Locate every blood parasite and identify its species.
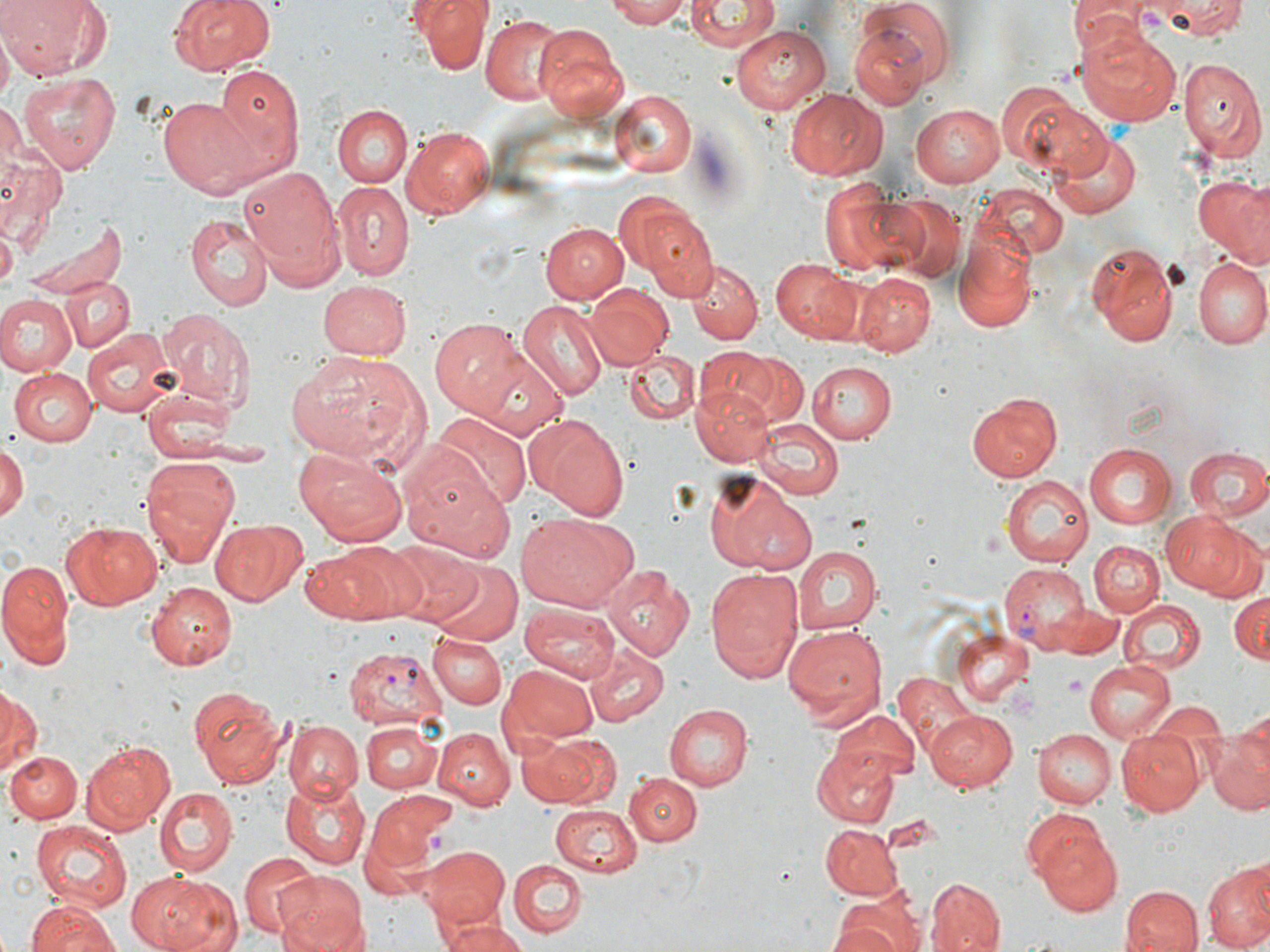

Approximate bounding boxes as named x1/y1/x2/y2 corners in pixels.
Plasmodium vivax-infected red blood cells: (x1=850, y1=26, x2=933, y2=109), (x1=999, y1=562, x2=1089, y2=648), (x1=343, y1=645, x2=447, y2=726).
No Plasmodium falciparum, Plasmodium ovale, Plasmodium malariae, Babesia divergens, or Trypanosoma brucei observed.

Summary:
  - Uninfected red blood cell locations: (x1=0, y1=0, x2=104, y2=79), (x1=169, y1=0, x2=277, y2=76), (x1=415, y1=0, x2=488, y2=74), (x1=604, y1=0, x2=691, y2=27), (x1=685, y1=0, x2=778, y2=50), (x1=1068, y1=0, x2=1147, y2=54), (x1=1145, y1=0, x2=1247, y2=39), (x1=860, y1=2, x2=959, y2=90), (x1=483, y1=16, x2=563, y2=104), (x1=536, y1=22, x2=628, y2=120), (x1=1077, y1=26, x2=1181, y2=128), (x1=732, y1=27, x2=829, y2=113), (x1=1178, y1=54, x2=1268, y2=164), (x1=213, y1=63, x2=305, y2=177), (x1=19, y1=72, x2=121, y2=174), (x1=994, y1=81, x2=1102, y2=176), (x1=786, y1=87, x2=890, y2=182), (x1=613, y1=89, x2=694, y2=174), (x1=158, y1=97, x2=262, y2=197), (x1=0, y1=101, x2=30, y2=184), (x1=910, y1=104, x2=1005, y2=186), (x1=333, y1=105, x2=412, y2=187), (x1=334, y1=112, x2=487, y2=198), (x1=401, y1=125, x2=496, y2=218), (x1=1048, y1=130, x2=1140, y2=221), (x1=0, y1=149, x2=67, y2=243), (x1=236, y1=165, x2=344, y2=285), (x1=1191, y1=173, x2=1268, y2=266), (x1=331, y1=183, x2=414, y2=282), (x1=820, y1=183, x2=918, y2=276), (x1=975, y1=184, x2=1068, y2=263), (x1=613, y1=189, x2=697, y2=275), (x1=882, y1=195, x2=966, y2=280), (x1=186, y1=212, x2=273, y2=311), (x1=22, y1=215, x2=132, y2=304), (x1=647, y1=216, x2=719, y2=296), (x1=541, y1=221, x2=629, y2=304), (x1=1, y1=226, x2=17, y2=285), (x1=953, y1=236, x2=1038, y2=334), (x1=1088, y1=241, x2=1179, y2=349), (x1=770, y1=258, x2=864, y2=345), (x1=685, y1=259, x2=762, y2=345), (x1=1192, y1=259, x2=1268, y2=350), (x1=853, y1=272, x2=936, y2=355), (x1=62, y1=277, x2=133, y2=350), (x1=317, y1=281, x2=411, y2=361), (x1=584, y1=284, x2=672, y2=370), (x1=0, y1=296, x2=76, y2=376), (x1=516, y1=301, x2=607, y2=401), (x1=156, y1=305, x2=254, y2=409), (x1=429, y1=317, x2=525, y2=416), (x1=83, y1=326, x2=177, y2=417), (x1=466, y1=345, x2=569, y2=440), (x1=625, y1=348, x2=700, y2=424), (x1=692, y1=348, x2=783, y2=424), (x1=285, y1=350, x2=425, y2=467), (x1=728, y1=351, x2=808, y2=427), (x1=806, y1=360, x2=897, y2=444), (x1=9, y1=369, x2=97, y2=445), (x1=694, y1=383, x2=774, y2=466), (x1=140, y1=389, x2=239, y2=462), (x1=963, y1=392, x2=1062, y2=483), (x1=429, y1=412, x2=530, y2=514), (x1=758, y1=420, x2=842, y2=498), (x1=534, y1=421, x2=628, y2=521), (x1=1086, y1=442, x2=1175, y2=529), (x1=0, y1=443, x2=26, y2=524), (x1=1185, y1=447, x2=1270, y2=521), (x1=295, y1=449, x2=407, y2=549), (x1=140, y1=460, x2=238, y2=566), (x1=401, y1=462, x2=519, y2=563), (x1=704, y1=473, x2=816, y2=575), (x1=1003, y1=474, x2=1096, y2=565), (x1=1163, y1=510, x2=1259, y2=596), (x1=516, y1=514, x2=629, y2=612), (x1=211, y1=518, x2=307, y2=608), (x1=61, y1=521, x2=162, y2=609), (x1=1089, y1=539, x2=1164, y2=617), (x1=335, y1=542, x2=433, y2=620), (x1=386, y1=542, x2=480, y2=623), (x1=298, y1=544, x2=400, y2=625), (x1=791, y1=547, x2=878, y2=634), (x1=0, y1=559, x2=72, y2=664), (x1=428, y1=561, x2=521, y2=645), (x1=602, y1=565, x2=695, y2=660), (x1=704, y1=566, x2=803, y2=682), (x1=147, y1=581, x2=242, y2=671), (x1=1229, y1=591, x2=1269, y2=665), (x1=1121, y1=597, x2=1204, y2=673), (x1=521, y1=604, x2=620, y2=682), (x1=1056, y1=607, x2=1123, y2=656), (x1=783, y1=622, x2=888, y2=730), (x1=952, y1=627, x2=1034, y2=707), (x1=429, y1=633, x2=506, y2=709), (x1=584, y1=646, x2=669, y2=725), (x1=1085, y1=658, x2=1176, y2=739), (x1=501, y1=666, x2=598, y2=743), (x1=891, y1=672, x2=977, y2=768), (x1=186, y1=683, x2=288, y2=786), (x1=0, y1=688, x2=40, y2=775), (x1=1145, y1=702, x2=1231, y2=737), (x1=663, y1=704, x2=752, y2=790), (x1=828, y1=709, x2=923, y2=784), (x1=928, y1=709, x2=1018, y2=792), (x1=283, y1=722, x2=364, y2=803), (x1=361, y1=722, x2=443, y2=794), (x1=1031, y1=728, x2=1115, y2=808), (x1=432, y1=729, x2=513, y2=809), (x1=1118, y1=731, x2=1204, y2=814), (x1=526, y1=734, x2=621, y2=808), (x1=1208, y1=736, x2=1270, y2=815), (x1=82, y1=740, x2=175, y2=831), (x1=813, y1=743, x2=904, y2=827), (x1=4, y1=751, x2=80, y2=823), (x1=626, y1=772, x2=702, y2=848), (x1=279, y1=779, x2=372, y2=868), (x1=154, y1=788, x2=237, y2=874), (x1=368, y1=792, x2=458, y2=872), (x1=551, y1=804, x2=644, y2=877), (x1=32, y1=820, x2=133, y2=911), (x1=821, y1=825, x2=904, y2=899), (x1=1032, y1=826, x2=1124, y2=916), (x1=423, y1=845, x2=511, y2=927), (x1=236, y1=853, x2=319, y2=937), (x1=507, y1=858, x2=587, y2=936), (x1=1203, y1=864, x2=1270, y2=952), (x1=129, y1=872, x2=237, y2=952), (x1=275, y1=872, x2=369, y2=952), (x1=926, y1=878, x2=1005, y2=951), (x1=425, y1=884, x2=517, y2=952), (x1=1118, y1=884, x2=1203, y2=952), (x1=829, y1=896, x2=923, y2=952), (x1=26, y1=898, x2=121, y2=952), (x1=433, y1=916, x2=527, y2=952)
  - Platelet locations: (x1=1004, y1=685, x2=1040, y2=720)
  - Slide-level diagnosis: Plasmodium vivax
  - Preparation: thin blood film
  - Stain: May-Grünwald-Giemsa
  - Field of view: single
  - Modality: optical microscopy
  - Magnification: 1000x
  - Image size: 1270×952 pixels